Classify this cell by malaria status.
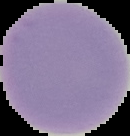
Uninfected.

image size = 130×136 pixels
preparation = thin blood film
image type = cell region segmented out of the field of view; surrounding area masked to black